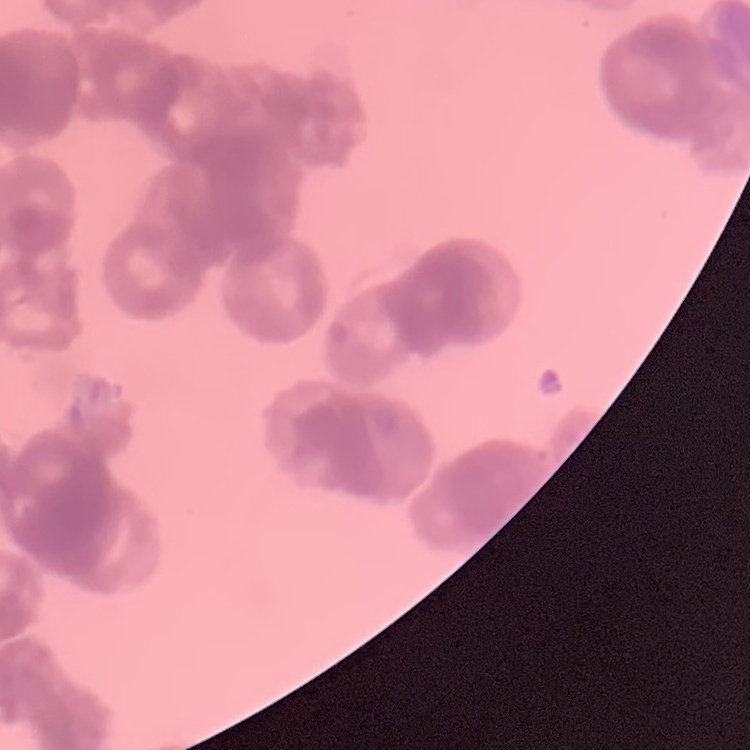

The erythrocytes exhibit rouleaux formation. Field's or Giemsa stain. One tile cut from a larger photomicrograph. Thin blood film.